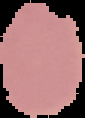
Image is 85×118 pixels. Result: no Plasmodium parasites seen. From a thin blood film. Cell region segmented out of the field of view; the surrounding area is masked to black.